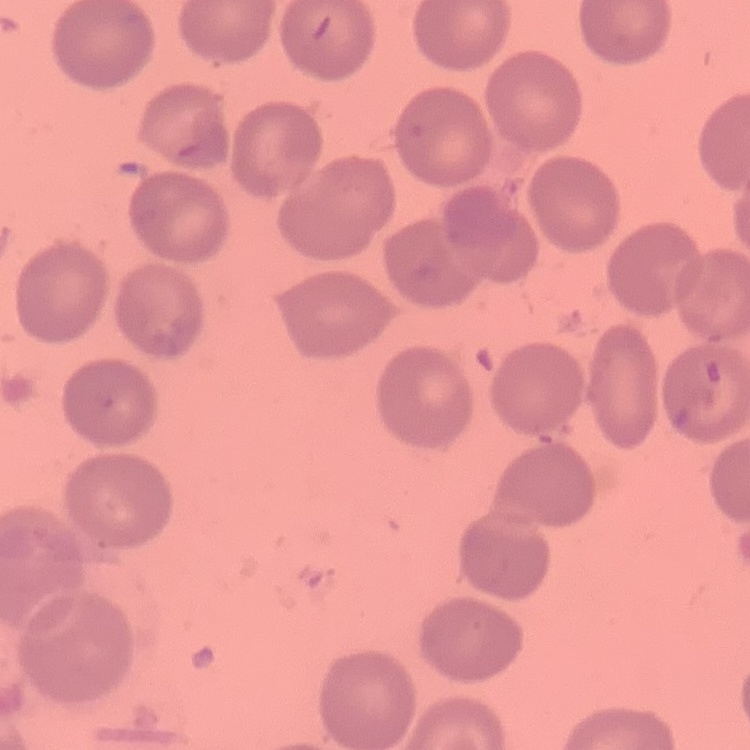

erythrocyte_morphology: no rouleaux formation
preparation: thin peripheral smear
image_type: square crop of a larger photomicrograph
stain: Field's or Giemsa